Report the malaria status of this cell.
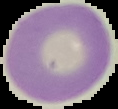

It is uninfected.

{
  "image_size": "118×109 pixels",
  "preparation": "thin blood smear",
  "image_type": "segmented cell region with the area outside set to black"
}